Assess the morphology of the erythrocytes.
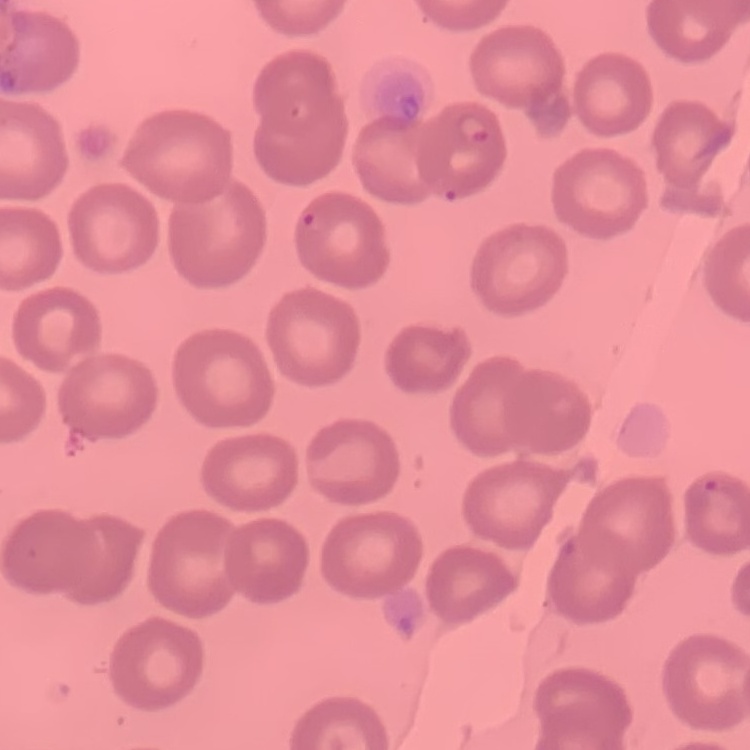
No rouleaux formation.

preparation = thin blood film
stain = Field's or Giemsa
image type = one tile cut from a larger photomicrograph